Assess the morphology of the erythrocytes.
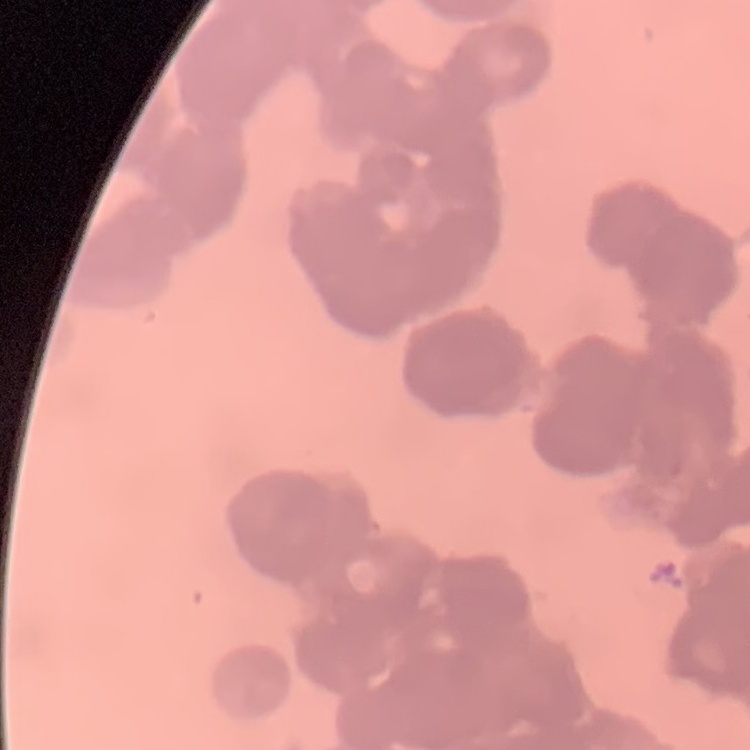

Rouleaux formation.

image_type: square crop of a larger photomicrograph
stain: Field's or Giemsa
preparation: thin blood film